Report the malaria status of this cell.
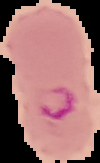

Parasitized.

Image is 100×163 pixels. Cell region segmented out of the field of view; the surrounding area is masked to black. From a thin blood smear.